State the blood parasite species.
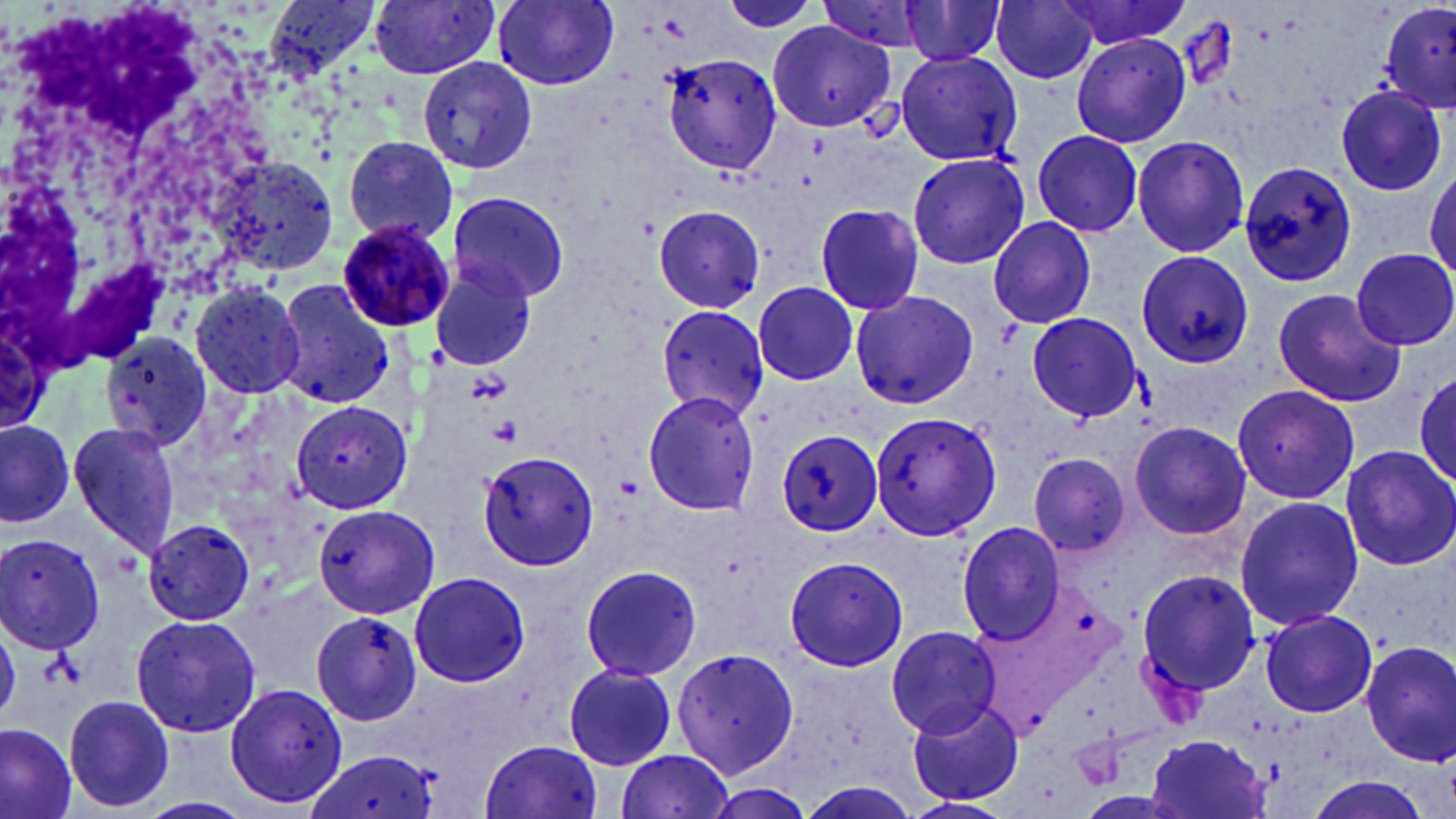

Plasmodium malariae.

Approximate bounding boxes as (x1, y1, x2, y2) in pixels. Platelet locations: (488, 414, 524, 446), (39, 650, 80, 690). Uninfected red blood cell locations: (265, 0, 382, 78), (369, 0, 503, 84), (491, 0, 621, 90), (990, 0, 1099, 86), (1055, 0, 1196, 53), (717, 1, 826, 38), (897, 1, 1007, 69), (1380, 1, 1455, 109), (768, 19, 894, 131), (1071, 33, 1192, 148), (661, 49, 782, 176), (897, 51, 1023, 168), (418, 55, 540, 175), (1335, 85, 1448, 197), (1032, 128, 1142, 237), (1131, 135, 1249, 257), (338, 137, 461, 244), (906, 152, 1028, 270), (208, 154, 340, 281), (1240, 158, 1358, 289), (1427, 166, 1456, 289), (447, 189, 571, 303), (651, 204, 765, 313), (811, 205, 929, 315), (989, 216, 1098, 330), (1352, 248, 1456, 349), (1135, 250, 1253, 367), (428, 255, 540, 373), (188, 280, 307, 399), (752, 280, 861, 387), (274, 281, 395, 406), (1272, 288, 1405, 408), (848, 289, 979, 411), (654, 305, 769, 422), (1026, 311, 1141, 422), (1259, 316, 1399, 473), (99, 331, 214, 452), (1412, 369, 1456, 489), (1231, 384, 1360, 503), (641, 392, 760, 516), (288, 399, 413, 514), (870, 411, 1001, 542), (0, 417, 77, 528), (67, 420, 182, 557), (1129, 421, 1254, 540), (772, 427, 885, 536), (1337, 445, 1456, 571), (477, 450, 600, 572), (1028, 452, 1131, 558), (1233, 495, 1364, 633), (314, 506, 441, 617), (140, 516, 257, 625), (955, 520, 1066, 644), (0, 533, 107, 652), (782, 555, 909, 673), (577, 564, 701, 682), (1136, 568, 1262, 699), (407, 571, 529, 686), (1259, 609, 1378, 717), (307, 611, 426, 725), (131, 613, 262, 739), (885, 625, 1003, 739), (0, 632, 26, 719), (1360, 641, 1456, 766), (673, 646, 800, 778), (562, 663, 679, 770), (222, 681, 349, 810), (62, 694, 176, 814), (907, 698, 1024, 807), (0, 721, 78, 819), (1146, 733, 1271, 818), (481, 738, 604, 819), (612, 749, 737, 819), (303, 751, 442, 819), (136, 796, 254, 819), (899, 797, 1014, 819). Plasmodium malariae-infected red blood cell locations: (332, 218, 454, 331). Light microscopy. One field of a larger specimen. Image is 1456×819 pixels. Thin blood film. Captured at 1000x magnification. May-Grünwald-Giemsa stain.